Comment on the morphology of the red blood cells.
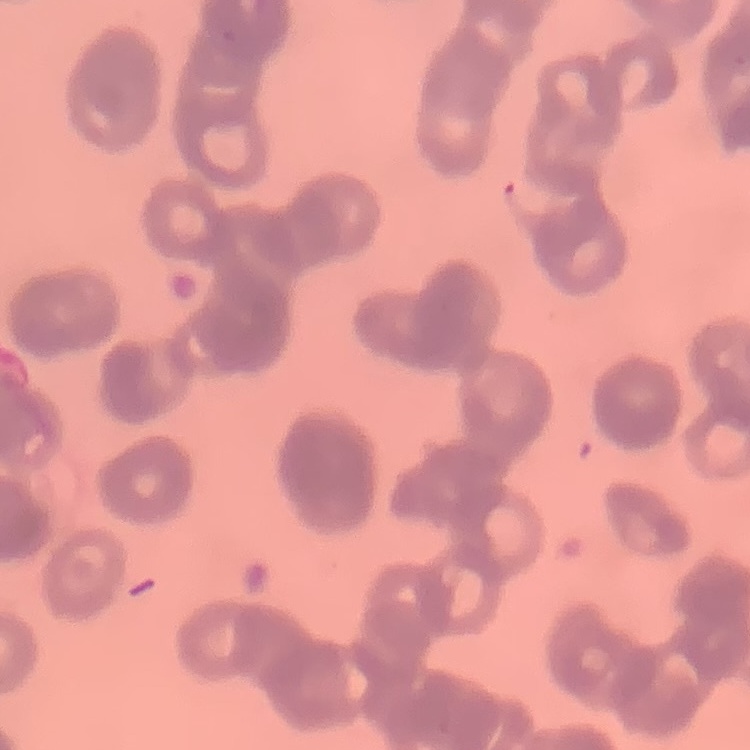
They show rouleaux formation.

Summary:
  - Preparation: thin peripheral smear
  - Image type: one tile cut from a larger photomicrograph
  - Stain: Field's or Giemsa